Outline each Plasmodium ovale-infected red blood cell.
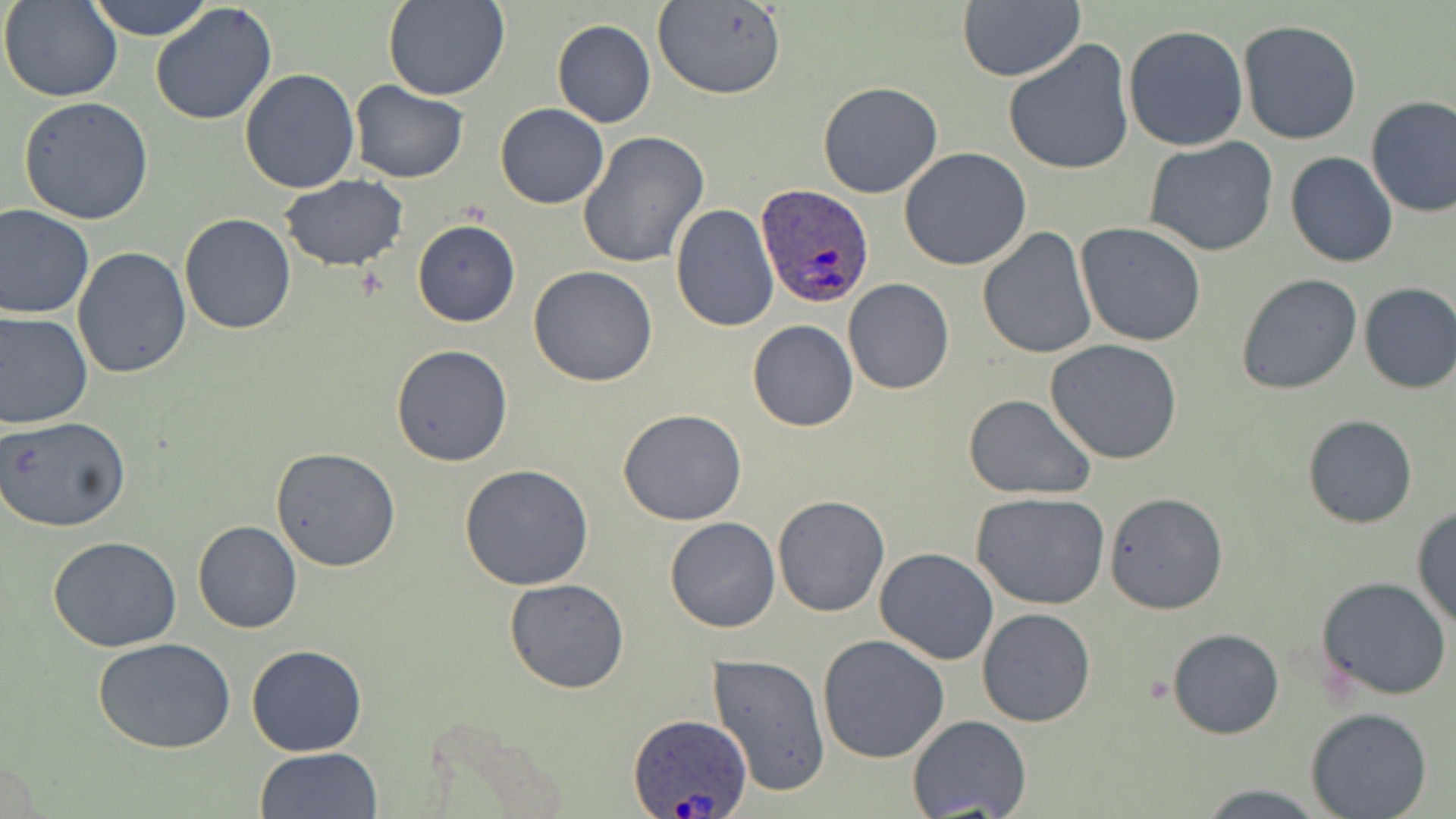
Approximate bounding boxes as (x1, y1, x2, y2) in pixels.
Plasmodium ovale-infected red blood cells: (755, 182, 875, 308), (626, 712, 753, 817).

Uninfected red blood cell locations: (1, 0, 124, 103), (87, 0, 216, 39), (382, 1, 512, 103), (957, 1, 1085, 83), (651, 2, 788, 100), (148, 3, 278, 126), (364, 9, 489, 185), (551, 19, 656, 128), (1238, 19, 1364, 145), (1123, 25, 1249, 151), (1004, 38, 1135, 176), (238, 68, 361, 193), (348, 82, 468, 182), (817, 82, 944, 198), (1364, 95, 1456, 219), (17, 96, 154, 226), (495, 103, 609, 209), (576, 132, 709, 269), (1142, 136, 1279, 257), (899, 147, 1032, 271), (1285, 151, 1398, 269), (280, 176, 408, 272), (0, 203, 94, 318), (669, 204, 779, 333), (178, 212, 298, 334), (411, 219, 520, 327), (1075, 223, 1207, 348), (977, 226, 1097, 360), (72, 247, 193, 379), (528, 265, 658, 387), (1235, 273, 1362, 395), (843, 278, 954, 395), (1357, 282, 1456, 394), (0, 310, 93, 430), (747, 319, 858, 432), (1046, 339, 1185, 465), (389, 344, 514, 467), (961, 393, 1096, 499), (618, 409, 748, 526), (1, 414, 131, 534), (1303, 415, 1417, 529), (272, 448, 401, 571), (459, 463, 593, 590), (1104, 492, 1227, 615), (972, 493, 1112, 609), (772, 495, 889, 617), (1411, 505, 1456, 630), (664, 517, 780, 633), (193, 521, 302, 634), (48, 536, 183, 653), (875, 547, 999, 665), (1315, 576, 1455, 701), (504, 577, 629, 694), (978, 608, 1096, 727), (1167, 627, 1284, 739), (817, 633, 950, 762), (92, 637, 237, 753), (246, 644, 367, 756), (709, 652, 831, 797), (1306, 708, 1434, 819), (906, 715, 1031, 819), (255, 747, 384, 819), (1192, 784, 1332, 817). Slide-level diagnosis: Plasmodium ovale. Thin blood smear. Captured at 1000x magnification. Light microscopy. Single field of view. Image is 1456×819 pixels. May-Grünwald-Giemsa-stained preparation.